Identify the parasite.
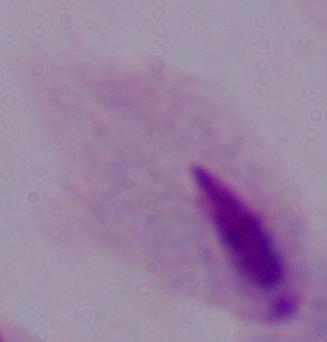

This is a trichomonad.

Captured at 1000x magnification. Micrograph.